Comment on the morphology of the erythrocytes.
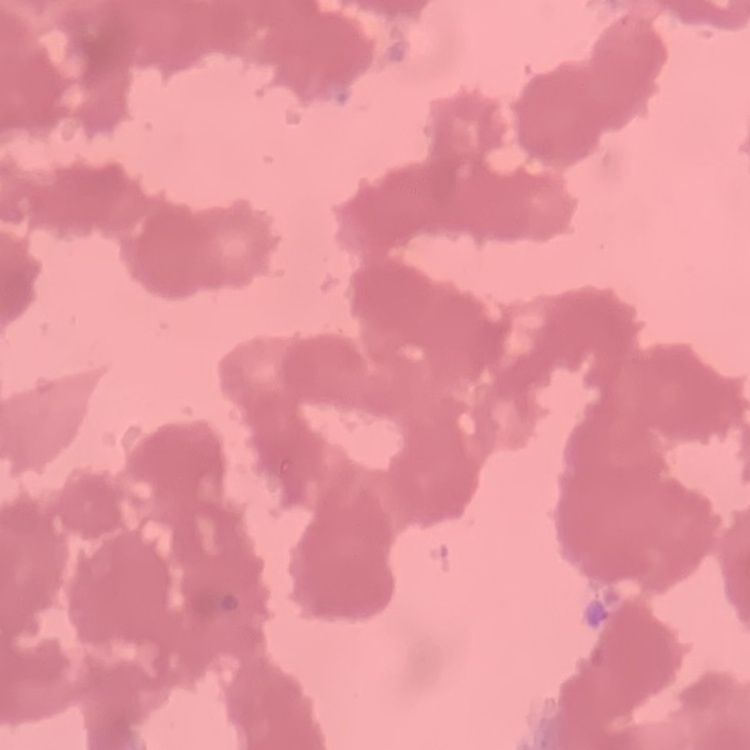
Rouleaux formation.

Field's or Giemsa stain. Thin peripheral smear. One tile cut from a larger photomicrograph.